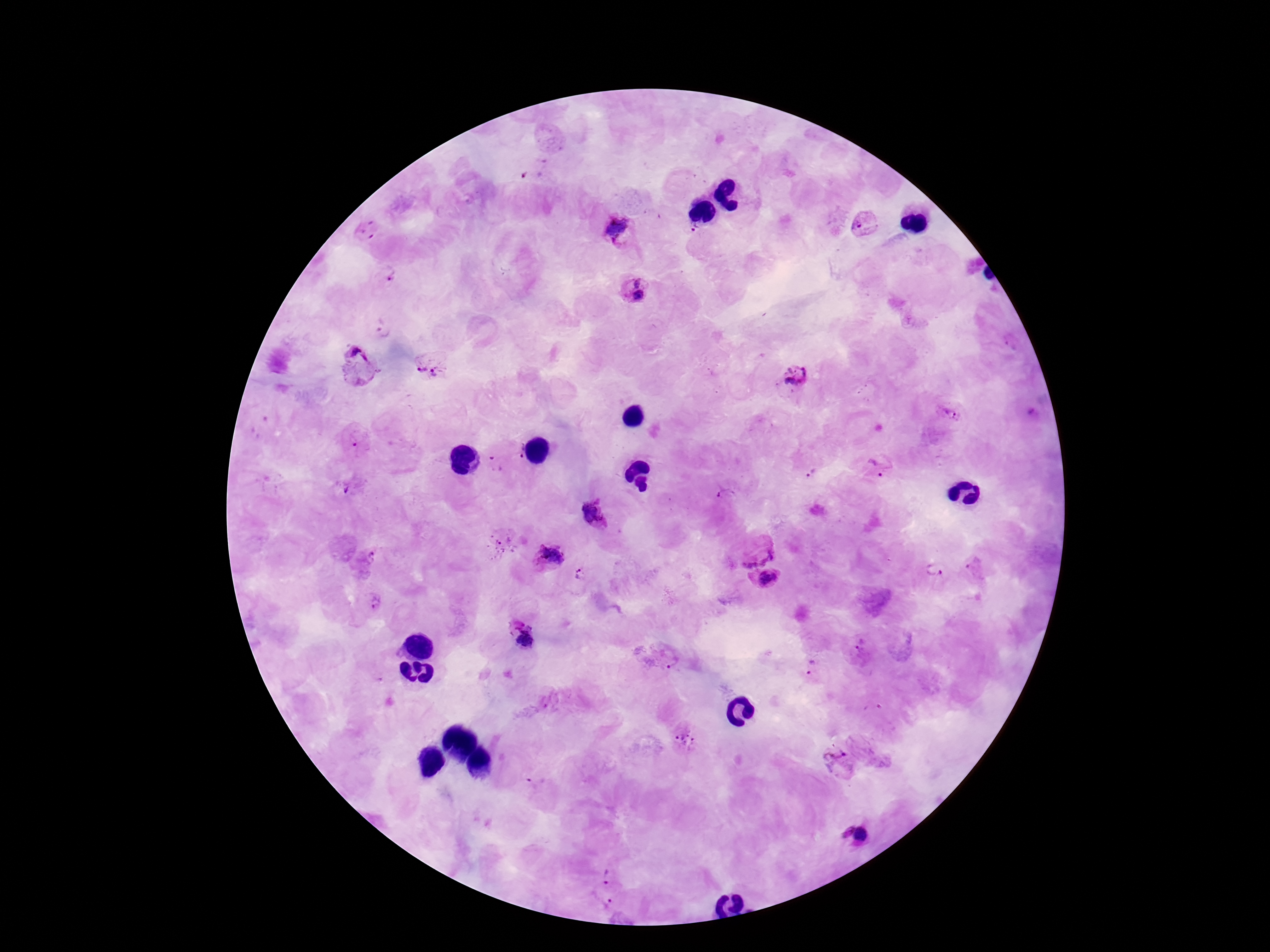
capture: smartphone camera through the microscope eyepiece
stain: Giemsa
patient_malaria_status: positive
field_of_view: single
magnification: 100x
image_size: 1270×952 pixels
plasmodium_parasite_locations: 'approximate centers as [x, y] in pixels: [533, 165], [863, 223], [365, 227], [619, 228], [694, 228], [387, 275], [635, 290], [383, 332], [432, 364], [358, 366], [793, 377], [948, 412], [1031, 414], [354, 439], [512, 446], [493, 464], [879, 465], [811, 473], [348, 488], [726, 496], [592, 514], [502, 542], [755, 548], [365, 559], [548, 559], [978, 568], [935, 570], [582, 575], [766, 580], [373, 600], [522, 633], [862, 652], [665, 658], [810, 667], [686, 739], [838, 763], [856, 835], [608, 875], [606, 904]'
preparation: thick blood smear